Locate and identify every blood parasite.
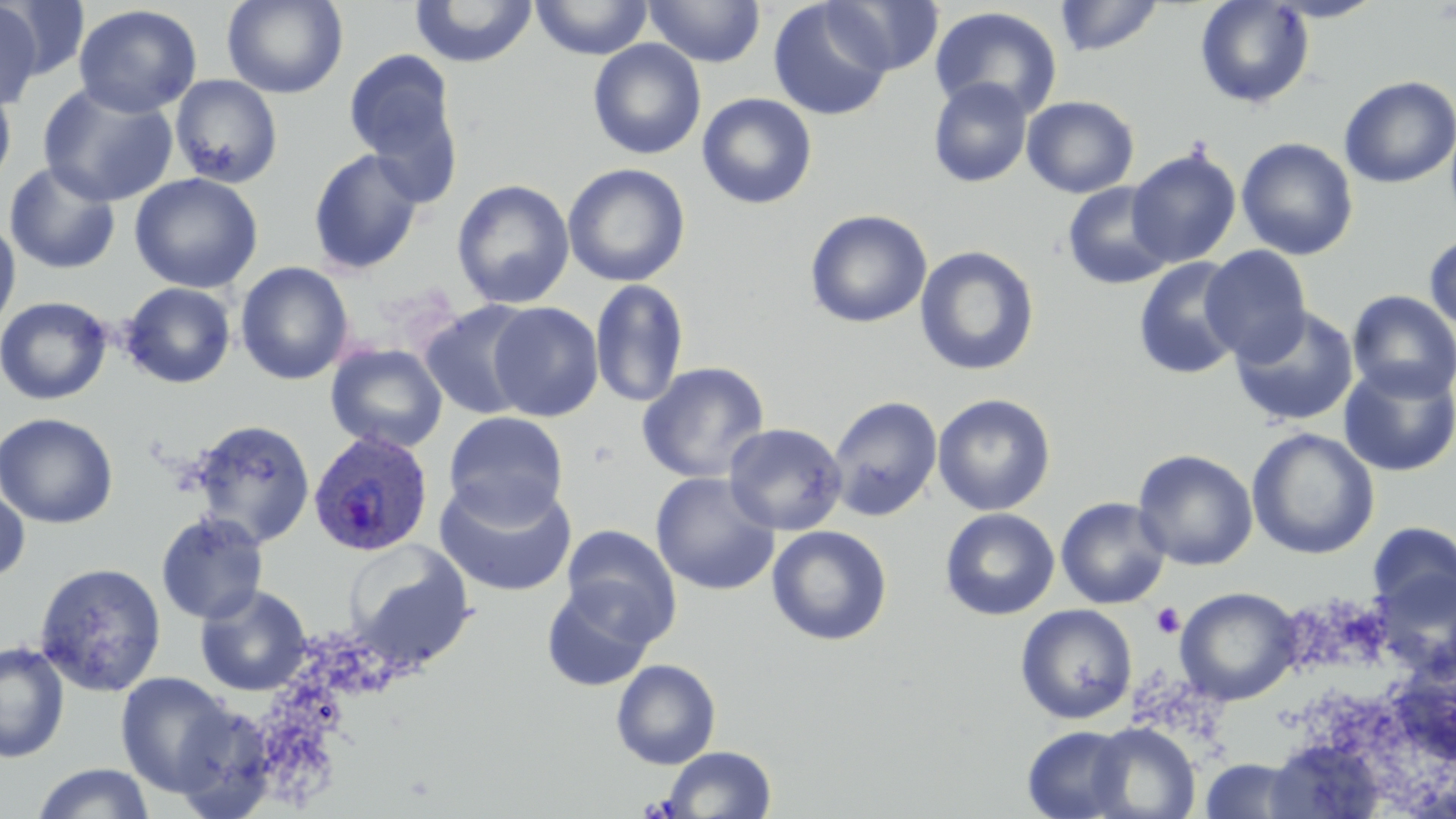
Approximate bounding boxes as (x1, y1, x2, y2) in pixels.
Plasmodium ovale-infected red blood cells: (307, 430, 435, 557).
No Plasmodium falciparum, Plasmodium malariae, Plasmodium vivax, Babesia divergens, or Trypanosoma brucei observed.

Platelet locations: (1151, 603, 1186, 638). Uninfected red blood cell locations: (3, 0, 93, 83), (221, 0, 349, 98), (409, 0, 538, 68), (531, 0, 652, 59), (643, 0, 766, 67), (823, 0, 945, 75), (1054, 0, 1164, 57), (1195, 0, 1314, 109), (1265, 0, 1387, 22), (0, 1, 44, 111), (769, 2, 892, 121), (73, 4, 202, 118), (929, 6, 1063, 120), (588, 39, 706, 160), (578, 42, 699, 288), (343, 48, 463, 199), (169, 74, 284, 189), (1338, 76, 1456, 189), (928, 78, 1033, 187), (37, 82, 179, 208), (0, 84, 16, 192), (697, 93, 817, 209), (1022, 95, 1139, 198), (1236, 137, 1358, 261), (1126, 147, 1242, 268), (307, 148, 425, 275), (3, 160, 121, 275), (562, 163, 690, 287), (129, 172, 264, 294), (452, 178, 575, 309), (1062, 180, 1177, 291), (804, 209, 933, 328), (0, 214, 21, 336), (1424, 232, 1456, 335), (914, 245, 1040, 377), (1200, 246, 1311, 365), (1133, 257, 1247, 379), (235, 262, 355, 386), (589, 279, 690, 409), (119, 282, 237, 389), (1346, 290, 1456, 402), (0, 296, 113, 406), (419, 300, 539, 420), (486, 302, 603, 422), (1229, 306, 1359, 428), (326, 343, 448, 454), (1337, 360, 1456, 477), (637, 361, 770, 484), (933, 393, 1056, 516), (828, 395, 943, 522), (443, 411, 569, 526), (0, 413, 119, 528), (188, 418, 316, 548), (723, 422, 847, 536), (1247, 428, 1380, 560), (1132, 449, 1258, 571), (650, 472, 780, 596), (434, 477, 577, 598), (0, 482, 31, 584), (1055, 497, 1171, 609), (939, 507, 1060, 621), (155, 511, 269, 625), (1367, 521, 1456, 618), (560, 525, 682, 644), (766, 525, 893, 646), (344, 539, 476, 671), (34, 561, 167, 697), (1370, 567, 1456, 684), (541, 583, 658, 692), (193, 584, 312, 696), (1175, 587, 1302, 705), (1015, 604, 1138, 724), (0, 641, 70, 763), (611, 659, 721, 770), (114, 671, 238, 797), (1086, 722, 1200, 819), (1022, 725, 1136, 818), (1265, 738, 1387, 819), (661, 746, 777, 818), (1197, 759, 1312, 818), (31, 763, 156, 819). Slide-level diagnosis: Plasmodium ovale. Image is 1456×819 pixels. Thin blood film. May-Grünwald-Giemsa-stained preparation. Light microscopy. Captured at 1000x magnification. One field of a larger specimen.